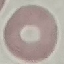

Summary:
  - Result: no malaria parasites detected
  - Image type: cell patch, automatically extracted from a larger field of view and resized to 64 × 64 pixels
  - Capture: smartphone through the microscope eyepiece
  - Preparation: thin smear
  - Stain: Giemsa